Comment on the morphology of the red blood cells.
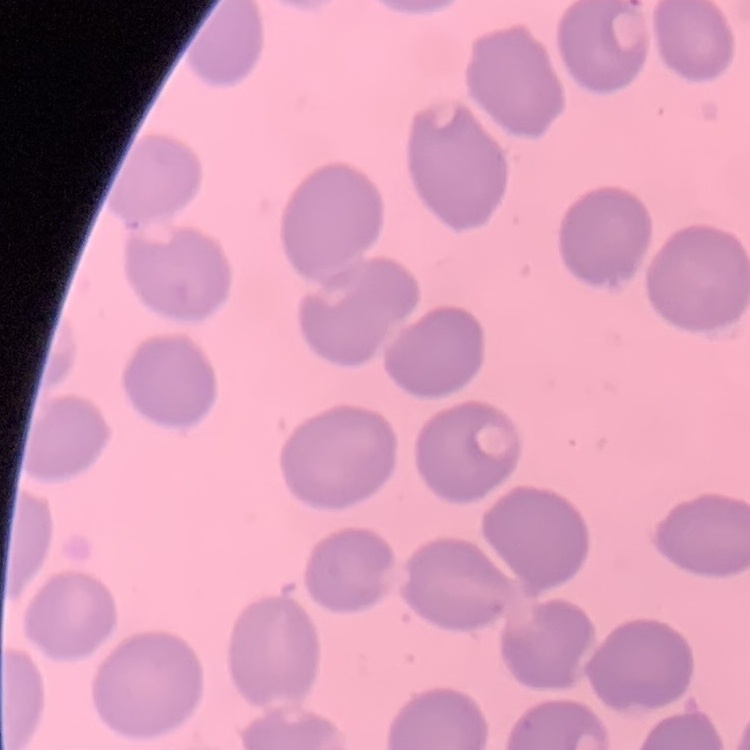
No rouleaux formation.

Field's or Giemsa stain. One tile cut from a larger photomicrograph. Thin blood smear.